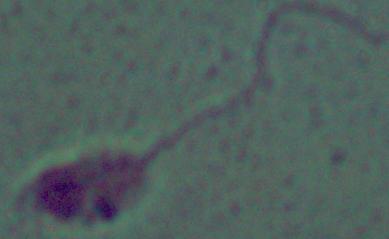

A Leishmania parasite is seen. 1000x magnification. Photomicrograph.